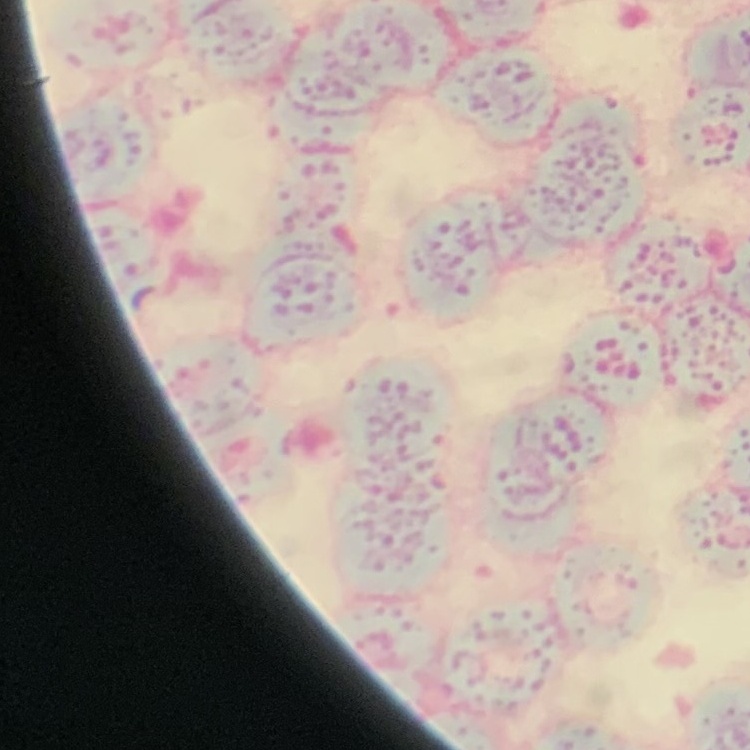

The erythrocytes show rouleaux formation. Thin blood film. Stained with either Field's or Giemsa. Square crop of a larger photomicrograph.